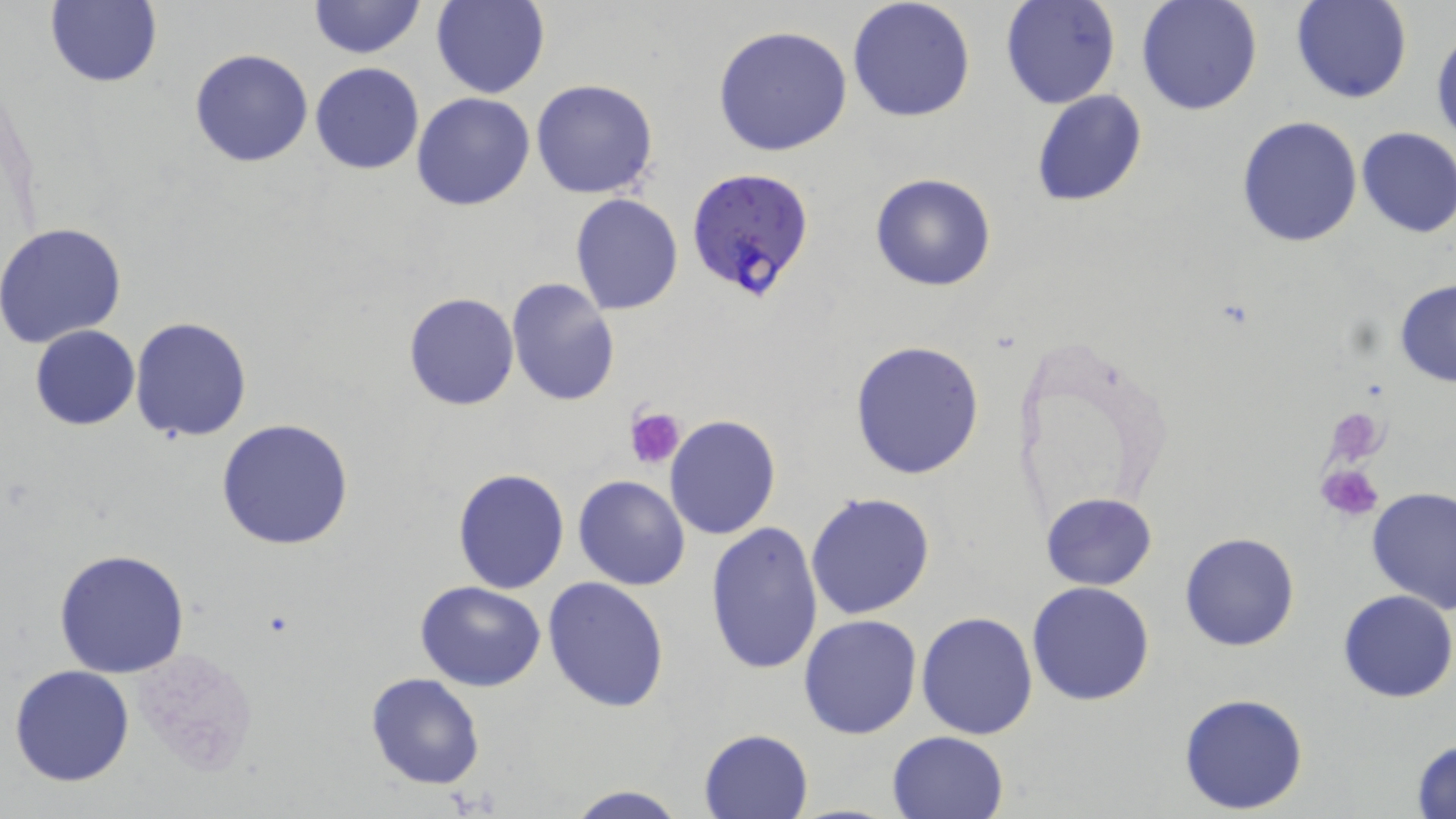

Summary:
  - Coordinate format: approximate bounding boxes as named x1/y1/x2/y2 corners in pixels
  - Platelet locations: (x1=625, y1=406, x2=685, y2=471), (x1=1316, y1=461, x2=1385, y2=521)
  - Uninfected red blood cell locations: (x1=847, y1=0, x2=976, y2=123), (x1=1000, y1=0, x2=1121, y2=110), (x1=1134, y1=0, x2=1262, y2=117), (x1=1290, y1=0, x2=1412, y2=105), (x1=45, y1=1, x2=163, y2=89), (x1=307, y1=1, x2=426, y2=59), (x1=431, y1=1, x2=549, y2=99), (x1=712, y1=25, x2=852, y2=157), (x1=1430, y1=31, x2=1456, y2=153), (x1=188, y1=47, x2=312, y2=168), (x1=309, y1=61, x2=425, y2=174), (x1=531, y1=79, x2=659, y2=200), (x1=1030, y1=89, x2=1146, y2=207), (x1=410, y1=92, x2=535, y2=212), (x1=1235, y1=116, x2=1364, y2=248), (x1=1355, y1=126, x2=1456, y2=237), (x1=868, y1=172, x2=997, y2=293), (x1=570, y1=194, x2=684, y2=315), (x1=0, y1=222, x2=128, y2=349), (x1=506, y1=277, x2=620, y2=406), (x1=1394, y1=281, x2=1456, y2=387), (x1=403, y1=293, x2=519, y2=411), (x1=130, y1=316, x2=252, y2=442), (x1=30, y1=325, x2=140, y2=430), (x1=849, y1=339, x2=988, y2=479), (x1=664, y1=414, x2=781, y2=540), (x1=215, y1=419, x2=355, y2=551), (x1=453, y1=467, x2=569, y2=594), (x1=572, y1=475, x2=690, y2=590), (x1=1365, y1=488, x2=1456, y2=611), (x1=804, y1=491, x2=936, y2=620), (x1=1041, y1=492, x2=1158, y2=589), (x1=703, y1=521, x2=823, y2=677), (x1=1179, y1=531, x2=1300, y2=650), (x1=53, y1=549, x2=191, y2=679), (x1=542, y1=577, x2=670, y2=712), (x1=415, y1=580, x2=548, y2=691), (x1=1026, y1=581, x2=1155, y2=705), (x1=1337, y1=590, x2=1455, y2=703), (x1=916, y1=611, x2=1039, y2=740), (x1=798, y1=614, x2=924, y2=739), (x1=8, y1=664, x2=136, y2=787), (x1=366, y1=672, x2=484, y2=790), (x1=1178, y1=692, x2=1309, y2=812), (x1=698, y1=728, x2=813, y2=818), (x1=887, y1=729, x2=1009, y2=819), (x1=1410, y1=737, x2=1456, y2=817), (x1=564, y1=785, x2=691, y2=819)
  - Plasmodium falciparum-infected red blood cell locations: (x1=685, y1=167, x2=817, y2=303)
  - Slide-level diagnosis: Plasmodium falciparum
  - Field of view: single
  - Preparation: thin blood smear
  - Image size: 1456×819 pixels
  - Modality: light microscopy
  - Magnification: 1000x
  - Stain: May-Grünwald-Giemsa